Report the malaria status of this cell.
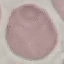
It is uninfected.

Giemsa stain. Thin blood film. Automatically extracted cell patch, resized to 64 × 64 pixels. Photographed with a smartphone camera at the microscope eyepiece.